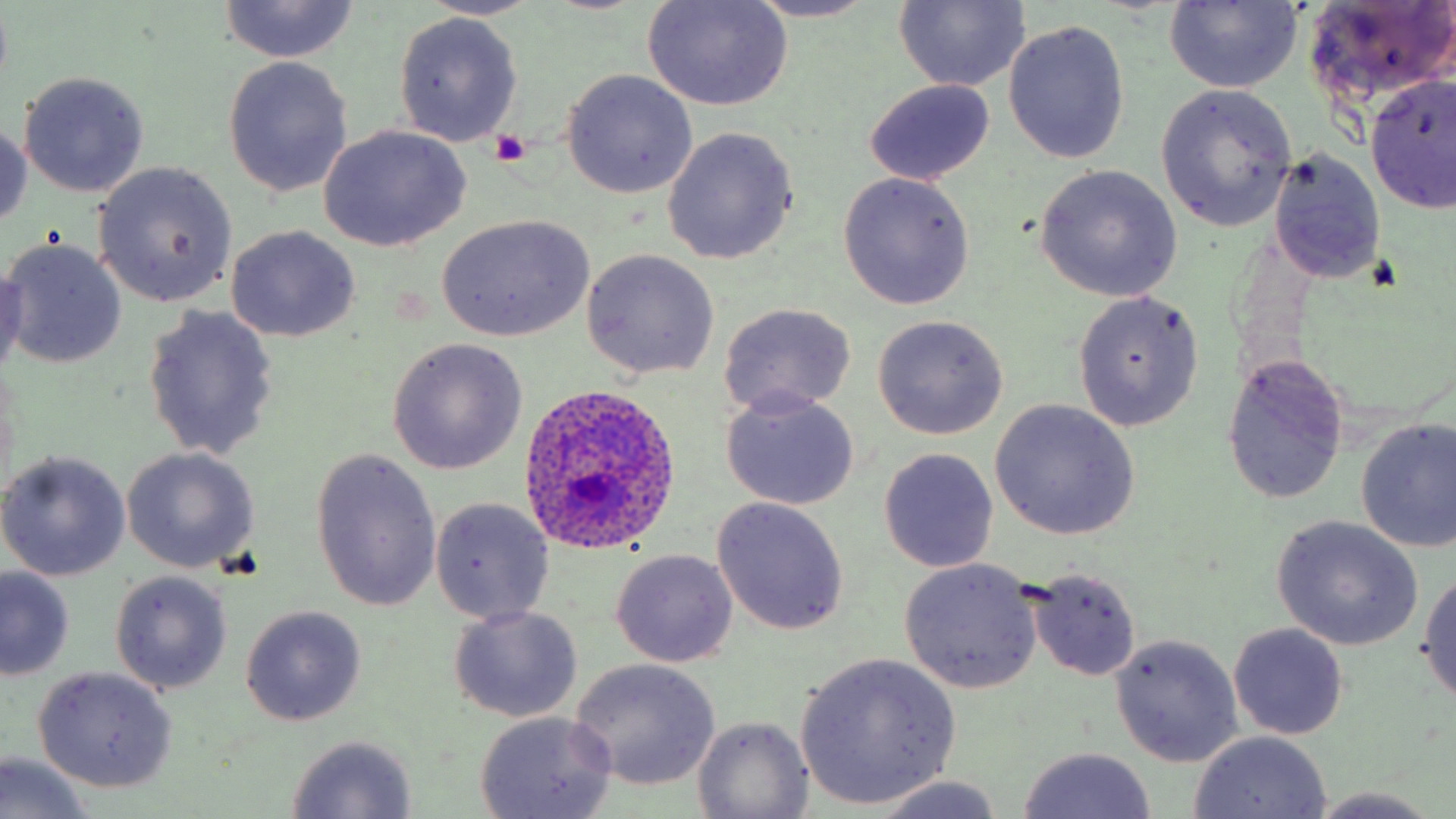
Approximate bounding boxes as named x1/y1/x2/y2 corners in pixels. Uninfected red blood cell locations: (x1=421, y1=0, x2=544, y2=21), (x1=643, y1=0, x2=794, y2=110), (x1=1303, y1=0, x2=1456, y2=106), (x1=217, y1=1, x2=361, y2=65), (x1=743, y1=1, x2=886, y2=23), (x1=894, y1=1, x2=1028, y2=91), (x1=1164, y1=1, x2=1302, y2=92), (x1=394, y1=13, x2=522, y2=145), (x1=1004, y1=20, x2=1128, y2=162), (x1=221, y1=56, x2=352, y2=197), (x1=561, y1=69, x2=698, y2=198), (x1=17, y1=71, x2=150, y2=197), (x1=1365, y1=73, x2=1456, y2=216), (x1=865, y1=78, x2=995, y2=185), (x1=1156, y1=84, x2=1298, y2=232), (x1=0, y1=116, x2=31, y2=235), (x1=317, y1=124, x2=471, y2=251), (x1=663, y1=128, x2=799, y2=265), (x1=1269, y1=148, x2=1386, y2=287), (x1=93, y1=161, x2=238, y2=308), (x1=1033, y1=166, x2=1183, y2=302), (x1=838, y1=172, x2=975, y2=308), (x1=437, y1=214, x2=594, y2=342), (x1=227, y1=225, x2=360, y2=342), (x1=2, y1=238, x2=127, y2=370), (x1=581, y1=248, x2=720, y2=379), (x1=0, y1=263, x2=27, y2=385), (x1=1072, y1=290, x2=1204, y2=432), (x1=719, y1=303, x2=857, y2=417), (x1=141, y1=305, x2=280, y2=460), (x1=871, y1=315, x2=1008, y2=440), (x1=385, y1=338, x2=527, y2=474), (x1=1221, y1=354, x2=1349, y2=506), (x1=721, y1=390, x2=858, y2=512), (x1=988, y1=400, x2=1140, y2=541), (x1=1354, y1=416, x2=1456, y2=552), (x1=121, y1=447, x2=259, y2=574), (x1=877, y1=447, x2=999, y2=574), (x1=309, y1=449, x2=443, y2=613), (x1=0, y1=450, x2=132, y2=581), (x1=711, y1=497, x2=849, y2=635), (x1=429, y1=498, x2=555, y2=624), (x1=1271, y1=516, x2=1425, y2=651), (x1=612, y1=548, x2=738, y2=668), (x1=900, y1=559, x2=1042, y2=693), (x1=0, y1=566, x2=74, y2=681), (x1=1417, y1=566, x2=1456, y2=706), (x1=1027, y1=569, x2=1143, y2=680), (x1=111, y1=571, x2=232, y2=694), (x1=239, y1=605, x2=367, y2=726), (x1=448, y1=606, x2=583, y2=724), (x1=1228, y1=623, x2=1350, y2=740), (x1=1109, y1=633, x2=1244, y2=767), (x1=795, y1=652, x2=961, y2=809), (x1=569, y1=658, x2=722, y2=791), (x1=32, y1=666, x2=178, y2=793), (x1=473, y1=710, x2=617, y2=819), (x1=694, y1=715, x2=813, y2=818), (x1=1188, y1=732, x2=1331, y2=817), (x1=285, y1=735, x2=419, y2=817), (x1=1017, y1=746, x2=1158, y2=819), (x1=1, y1=751, x2=95, y2=819), (x1=869, y1=775, x2=1012, y2=818), (x1=1302, y1=788, x2=1451, y2=817). Plasmodium ovale-infected red blood cell locations: (x1=517, y1=381, x2=681, y2=556). Platelet locations: (x1=490, y1=130, x2=530, y2=166). Slide-level diagnosis: Plasmodium ovale. May-Grünwald-Giemsa stain. Thin blood smear. Single field of view. Captured at 1000x magnification. Light microscopy. Image is 1456×819 pixels.